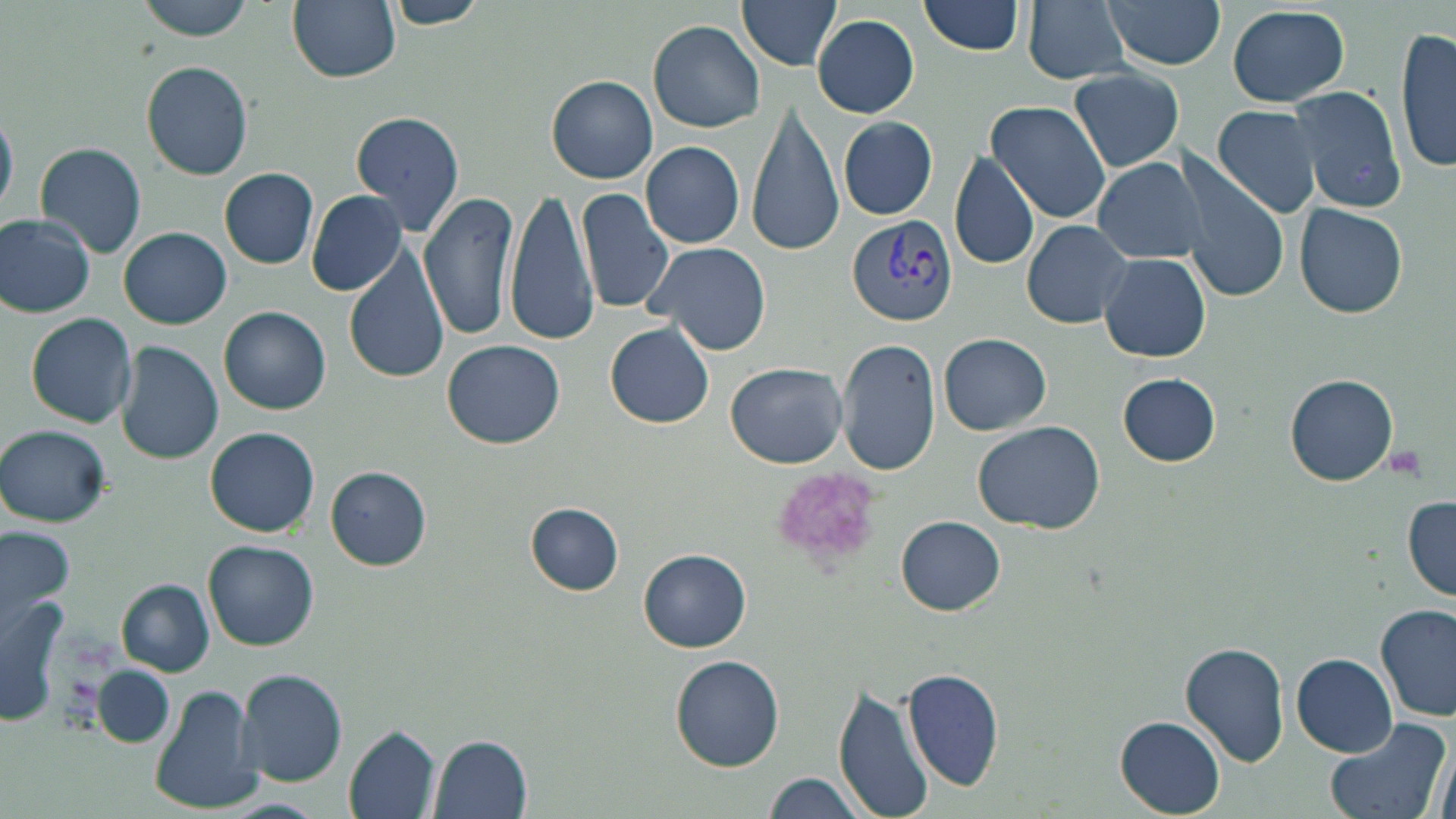

Summary:
  - Coordinate format: approximate bounding boxes as named x1/y1/x2/y2 corners in pixels
  - Uninfected red blood cell locations: (x1=134, y1=0, x2=258, y2=42), (x1=288, y1=0, x2=400, y2=84), (x1=380, y1=0, x2=492, y2=29), (x1=736, y1=0, x2=845, y2=70), (x1=918, y1=0, x2=1029, y2=56), (x1=1022, y1=0, x2=1133, y2=85), (x1=1102, y1=0, x2=1227, y2=70), (x1=1225, y1=4, x2=1351, y2=108), (x1=812, y1=15, x2=920, y2=117), (x1=648, y1=19, x2=766, y2=133), (x1=1396, y1=21, x2=1455, y2=176), (x1=143, y1=62, x2=253, y2=180), (x1=1066, y1=68, x2=1186, y2=172), (x1=547, y1=74, x2=658, y2=183), (x1=1286, y1=85, x2=1408, y2=214), (x1=745, y1=101, x2=845, y2=256), (x1=985, y1=101, x2=1111, y2=222), (x1=1214, y1=106, x2=1319, y2=218), (x1=0, y1=109, x2=17, y2=219), (x1=350, y1=111, x2=466, y2=236), (x1=838, y1=116, x2=938, y2=220), (x1=34, y1=141, x2=147, y2=258), (x1=641, y1=141, x2=747, y2=248), (x1=949, y1=150, x2=1042, y2=270), (x1=1172, y1=150, x2=1291, y2=302), (x1=1092, y1=155, x2=1207, y2=263), (x1=220, y1=168, x2=318, y2=268), (x1=505, y1=185, x2=602, y2=348), (x1=576, y1=187, x2=679, y2=318), (x1=421, y1=190, x2=520, y2=340), (x1=307, y1=191, x2=406, y2=295), (x1=1294, y1=204, x2=1409, y2=319), (x1=1, y1=214, x2=97, y2=317), (x1=1022, y1=219, x2=1135, y2=329), (x1=120, y1=226, x2=232, y2=329), (x1=644, y1=241, x2=770, y2=355), (x1=344, y1=246, x2=449, y2=384), (x1=1100, y1=253, x2=1211, y2=363), (x1=220, y1=306, x2=331, y2=415), (x1=25, y1=312, x2=137, y2=428), (x1=604, y1=321, x2=715, y2=429), (x1=939, y1=333, x2=1050, y2=434), (x1=838, y1=338, x2=941, y2=475), (x1=442, y1=340, x2=567, y2=449), (x1=116, y1=341, x2=224, y2=466), (x1=726, y1=361, x2=848, y2=469), (x1=1117, y1=372, x2=1223, y2=467), (x1=1286, y1=374, x2=1398, y2=484), (x1=973, y1=421, x2=1106, y2=534), (x1=1, y1=424, x2=113, y2=526), (x1=206, y1=427, x2=320, y2=537), (x1=327, y1=468, x2=432, y2=571), (x1=1403, y1=495, x2=1456, y2=600), (x1=526, y1=504, x2=624, y2=594), (x1=896, y1=515, x2=1005, y2=615), (x1=0, y1=525, x2=72, y2=639), (x1=203, y1=541, x2=318, y2=651), (x1=640, y1=549, x2=752, y2=652), (x1=118, y1=581, x2=214, y2=676), (x1=1, y1=591, x2=74, y2=724), (x1=1378, y1=604, x2=1456, y2=723), (x1=1180, y1=641, x2=1290, y2=767), (x1=670, y1=654, x2=786, y2=771), (x1=1293, y1=654, x2=1397, y2=756), (x1=94, y1=666, x2=176, y2=749), (x1=902, y1=667, x2=1005, y2=791), (x1=235, y1=668, x2=347, y2=787), (x1=834, y1=684, x2=935, y2=819), (x1=151, y1=685, x2=261, y2=813), (x1=1116, y1=715, x2=1225, y2=816), (x1=1322, y1=715, x2=1452, y2=819), (x1=345, y1=724, x2=443, y2=819), (x1=428, y1=733, x2=531, y2=817), (x1=762, y1=772, x2=871, y2=819)
  - Platelet locations: (x1=1381, y1=447, x2=1430, y2=482), (x1=770, y1=464, x2=883, y2=567)
  - Plasmodium vivax-infected red blood cell locations: (x1=847, y1=215, x2=960, y2=328)
  - Slide-level diagnosis: Plasmodium vivax
  - Modality: light microscopy
  - Magnification: 1000x
  - Field of view: one of a larger specimen
  - Preparation: thin blood smear
  - Image size: 1456×819 pixels
  - Stain: May-Grünwald-Giemsa